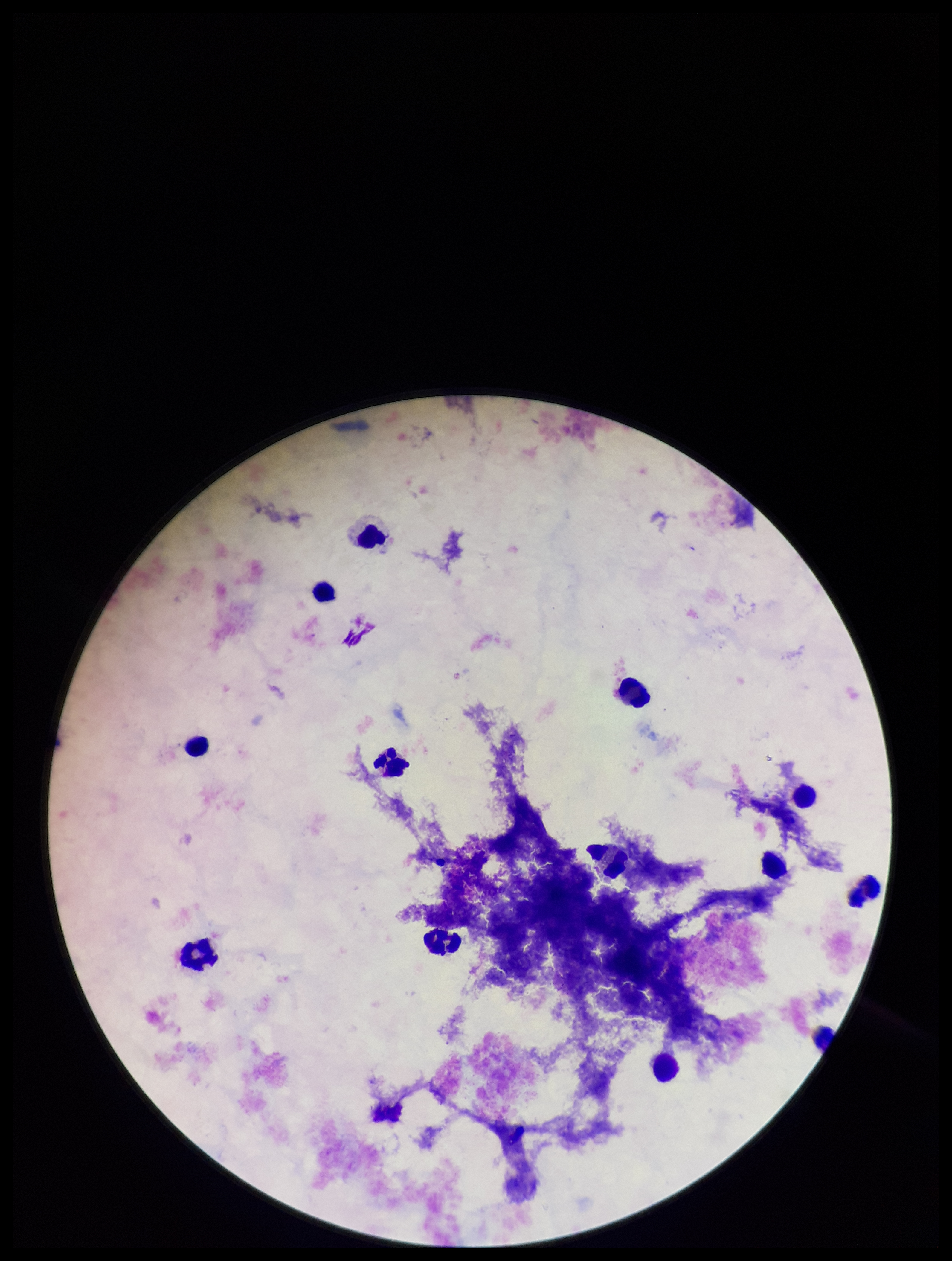

stain = Giemsa
image size = 952×1261 pixels
Plasmodium parasites = none identified
capture = smartphone photograph through the microscope eyepiece
field of view = single
parasite count = 0
preparation = thick blood smear
leukocyte count = 12
patient malaria status = negative